Classify this cell by malaria status.
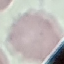
It is uninfected.

Acquired by smartphone through the microscope eyepiece. Cell patch, automatically extracted from a larger field of view and resized to 64 × 64 pixels. Giemsa stain. Thin blood smear.